Give the extent of all Plasmodium falciparum-infected red blood cells.
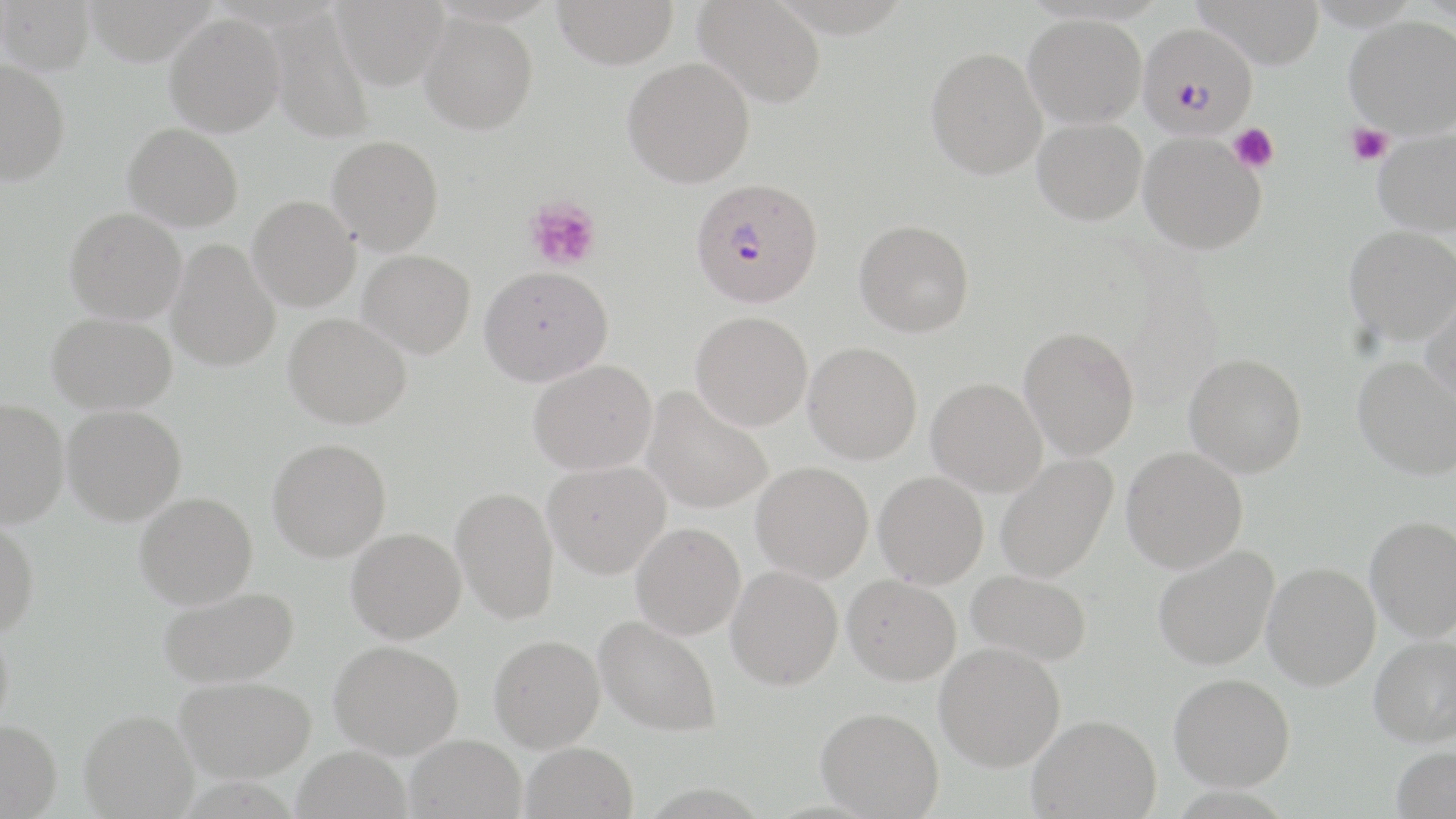
Approximate bounding boxes as (x1, y1, x2, y2) in pixels.
Plasmodium falciparum-infected red blood cells: (1138, 22, 1258, 138), (688, 176, 823, 306).

slide-level diagnosis = Plasmodium falciparum
preparation = thin blood film
field of view = single
stain = May-Grünwald-Giemsa
image size = 1456×819 pixels
modality = optical microscopy
uninfected red blood cell locations = approximate bounding boxes as (x1, y1, x2, y2) in pixels: (1, 0, 95, 75), (331, 0, 449, 90), (553, 0, 680, 69), (694, 0, 826, 106), (1193, 0, 1326, 69), (269, 9, 375, 143), (420, 13, 538, 135), (165, 14, 285, 136), (1024, 14, 1146, 129), (1344, 16, 1456, 137), (926, 46, 1048, 179), (622, 58, 755, 188), (0, 60, 70, 186), (1032, 118, 1147, 225), (123, 123, 243, 230), (1373, 127, 1456, 237), (1138, 132, 1267, 255), (327, 135, 443, 253), (247, 196, 360, 311), (65, 207, 186, 323), (854, 219, 975, 337), (1344, 225, 1456, 345), (166, 239, 280, 371), (358, 249, 476, 357), (479, 265, 613, 386), (1421, 287, 1456, 406), (47, 312, 177, 414), (691, 312, 813, 430), (283, 313, 412, 428), (1018, 326, 1139, 460), (803, 342, 922, 464), (1184, 353, 1307, 478), (1353, 355, 1455, 480), (528, 360, 657, 475), (926, 378, 1047, 496), (641, 387, 773, 514), (0, 398, 69, 528), (62, 405, 186, 525), (267, 438, 391, 561), (1122, 446, 1248, 573), (995, 454, 1118, 583), (543, 461, 670, 578), (751, 462, 873, 583), (874, 471, 988, 589), (451, 486, 559, 624), (135, 492, 257, 609), (1366, 515, 1456, 641), (0, 518, 40, 637), (630, 522, 746, 640), (346, 527, 465, 643), (1153, 545, 1279, 670), (1262, 562, 1381, 690), (725, 565, 843, 690), (966, 570, 1092, 665), (843, 575, 961, 685), (158, 586, 299, 688), (594, 615, 722, 737), (0, 624, 13, 734), (489, 634, 605, 752), (1368, 635, 1456, 746), (330, 640, 463, 758), (935, 642, 1065, 771), (1169, 672, 1295, 791), (176, 676, 316, 782), (816, 706, 943, 818), (80, 710, 198, 818), (1028, 714, 1161, 818), (0, 720, 62, 819), (406, 734, 527, 819), (521, 742, 638, 819), (1391, 745, 1456, 819), (292, 746, 412, 819)
magnification = 1000x
platelet locations = approximate bounding boxes as (x1, y1, x2, y2) in pixels: (1346, 123, 1393, 166), (1228, 124, 1279, 174), (525, 197, 602, 272)